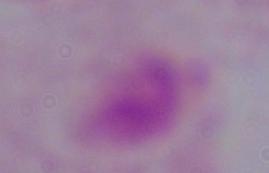
Summary:
  - Identification: trichomonad
  - Modality: micrograph
  - Magnification: 1000x